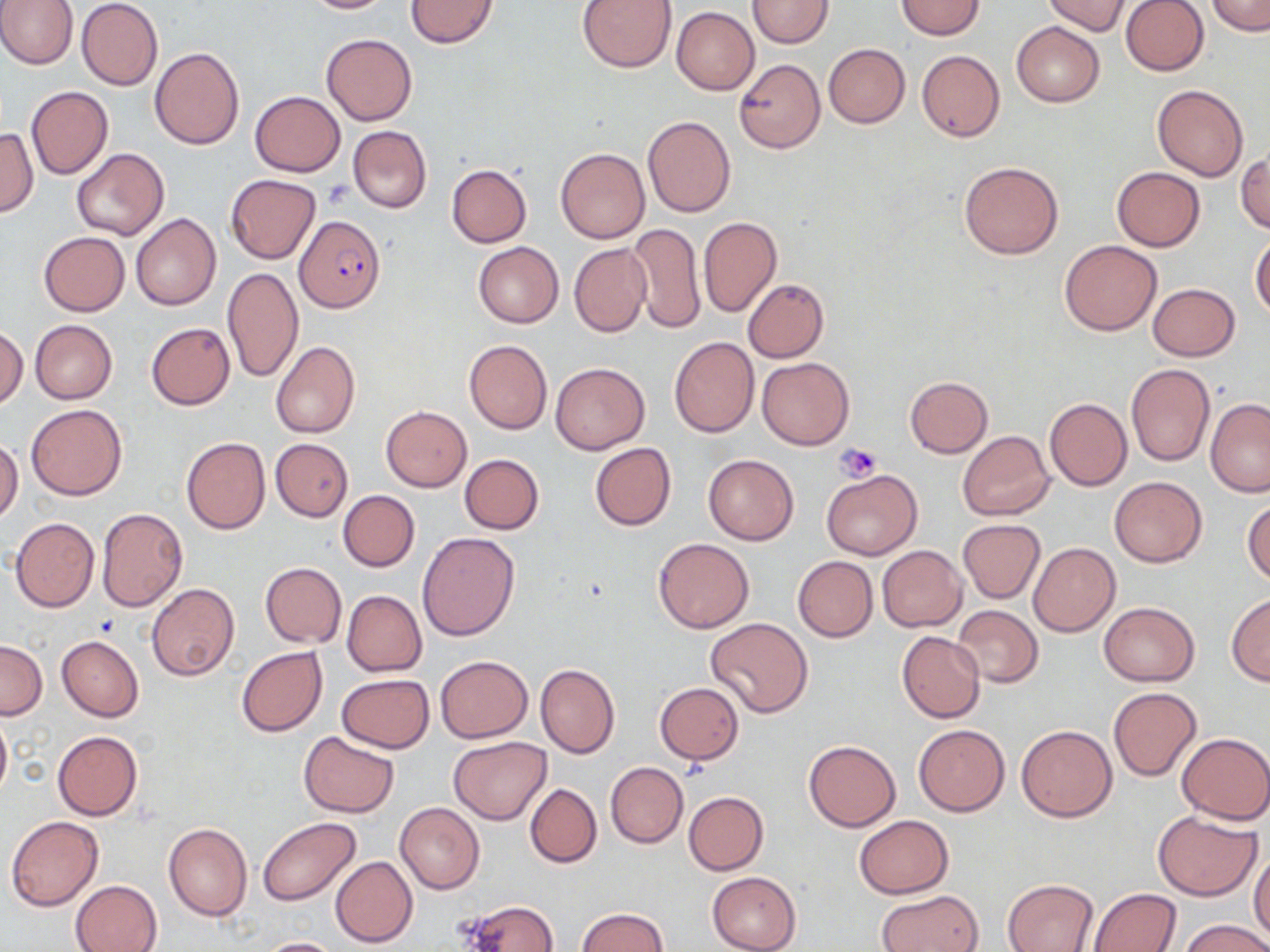

Summary:
  - Coordinate format: approximate bounding boxes as (x1,y1)-(x2,y2) corner pairs in pixels
  - Plasmodium falciparum-infected red blood cell locations: (296,217)-(385,312)
  - Uninfected red blood cell locations: (0,0)-(78,70), (76,0)-(162,90), (299,0)-(394,13), (404,0)-(499,49), (577,0)-(677,73), (747,0)-(833,48), (1041,0)-(1132,35), (1120,0)-(1208,75), (1206,0)-(1268,34), (895,1)-(985,39), (672,7)-(759,95), (1011,21)-(1105,107), (321,33)-(416,126), (823,43)-(910,128), (150,47)-(244,151), (916,50)-(1005,142), (735,58)-(825,153), (1152,83)-(1249,181), (25,85)-(113,180), (251,90)-(345,176), (642,115)-(736,217), (347,125)-(432,214), (0,128)-(37,216), (555,146)-(650,244), (71,148)-(169,242), (1236,153)-(1269,234), (959,161)-(1064,259), (446,164)-(532,247), (1112,166)-(1205,251), (226,175)-(320,264), (131,213)-(222,311), (698,217)-(782,316), (629,223)-(706,333), (39,232)-(128,315), (1251,233)-(1270,319), (1058,240)-(1162,336), (473,242)-(563,327), (569,243)-(650,336), (222,267)-(303,381), (742,278)-(829,364), (1148,283)-(1240,360), (30,320)-(117,404), (147,322)-(234,409), (0,326)-(28,410), (668,336)-(760,437), (464,338)-(553,434), (271,340)-(361,439), (758,356)-(853,451), (550,362)-(650,454), (1126,364)-(1216,468), (905,376)-(993,457), (1044,398)-(1132,491), (1205,399)-(1270,497), (27,403)-(126,500), (381,406)-(471,490), (957,430)-(1055,521), (181,436)-(270,534), (0,439)-(24,523), (271,439)-(354,521), (590,442)-(676,530), (460,454)-(543,534), (703,455)-(799,545), (822,468)-(921,560), (1109,476)-(1207,567), (338,490)-(419,572), (1244,500)-(1270,585), (97,508)-(187,612), (11,518)-(99,612), (957,519)-(1046,603), (417,531)-(521,640), (653,538)-(753,633), (1028,543)-(1121,636), (877,546)-(966,631), (792,556)-(877,642), (260,562)-(346,647), (146,583)-(239,680), (342,590)-(427,675), (1226,593)-(1270,685), (1099,601)-(1200,686), (953,605)-(1042,688), (704,619)-(814,718), (896,631)-(985,723), (57,636)-(144,721), (0,640)-(46,719), (236,646)-(327,737), (434,655)-(533,742), (536,663)-(619,759), (337,674)-(434,753), (654,683)-(745,764), (1108,687)-(1200,780), (0,708)-(11,803), (912,722)-(1010,816), (1017,724)-(1117,822), (53,730)-(143,819), (299,730)-(399,817), (1177,732)-(1270,824), (449,737)-(552,824), (803,740)-(901,832), (605,762)-(688,848), (525,784)-(602,868), (684,791)-(769,875), (394,803)-(485,893), (1153,811)-(1261,900), (6,814)-(104,912), (854,816)-(954,898), (258,818)-(361,906), (163,822)-(253,922), (1249,850)-(1270,946), (330,856)-(419,947), (706,871)-(803,952), (1004,878)-(1098,952), (70,880)-(162,952), (1089,887)-(1183,951), (874,889)-(984,952), (460,900)-(559,951), (575,908)-(670,952), (1180,919)-(1270,952), (256,937)-(343,951)
  - Platelet locations: (835,444)-(882,482)
  - Slide-level diagnosis: Plasmodium falciparum
  - Image size: 1270×952 pixels
  - Magnification: 1000x
  - Field of view: one of a larger specimen
  - Stain: May-Grünwald-Giemsa
  - Modality: light microscopy
  - Preparation: thin blood film